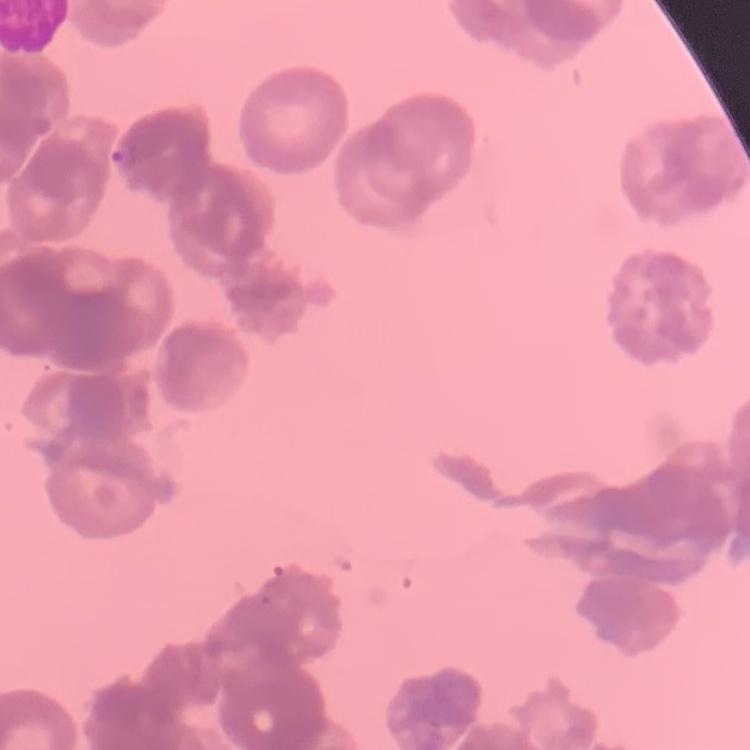

Summary:
  - Erythrocyte morphology: rouleaux formation
  - Preparation: thin peripheral smear
  - Image type: square crop of a larger photomicrograph
  - Stain: Field's or Giemsa